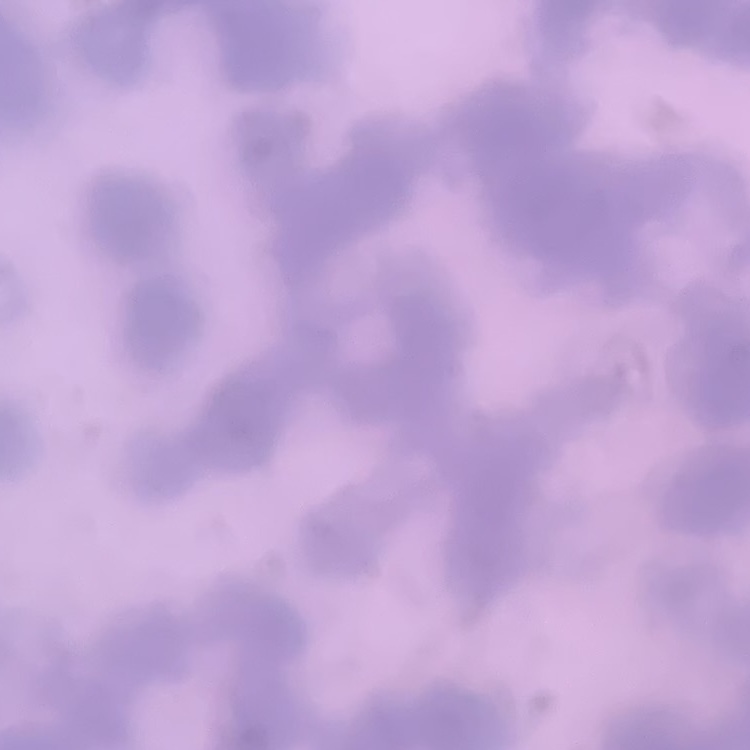 The erythrocytes show rouleaux formation. One tile cut from a larger photomicrograph. Field's or Giemsa stain. Thin peripheral smear.